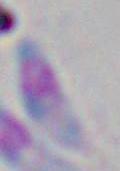
{
  "magnification": "1000x",
  "identification": "Toxoplasma gondii",
  "modality": "micrograph"
}